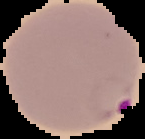
Summary:
  - Image type: cell region segmented out of the field of view; surrounding area masked to black
  - Image size: 145×139 pixels
  - Result: Plasmodium parasites identified
  - Preparation: thin blood film